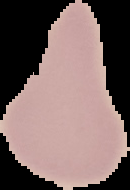

From a thin blood smear. Segmented cell region on a black background. Result: negative for Plasmodium parasites. Image is 130×190 pixels.